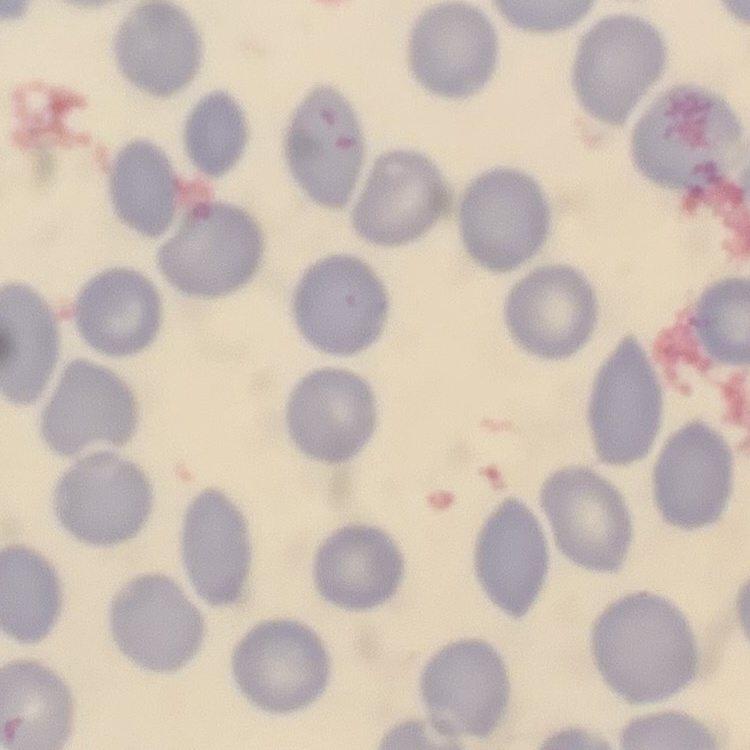

The red blood cells show no rouleaux formation. Thin blood smear. Stained with either Field's or Giemsa. Square crop of a larger photomicrograph.